Draw a bounding box around every malaria parasite, every leukocyte, and every artifact (stain precipitate or debris).
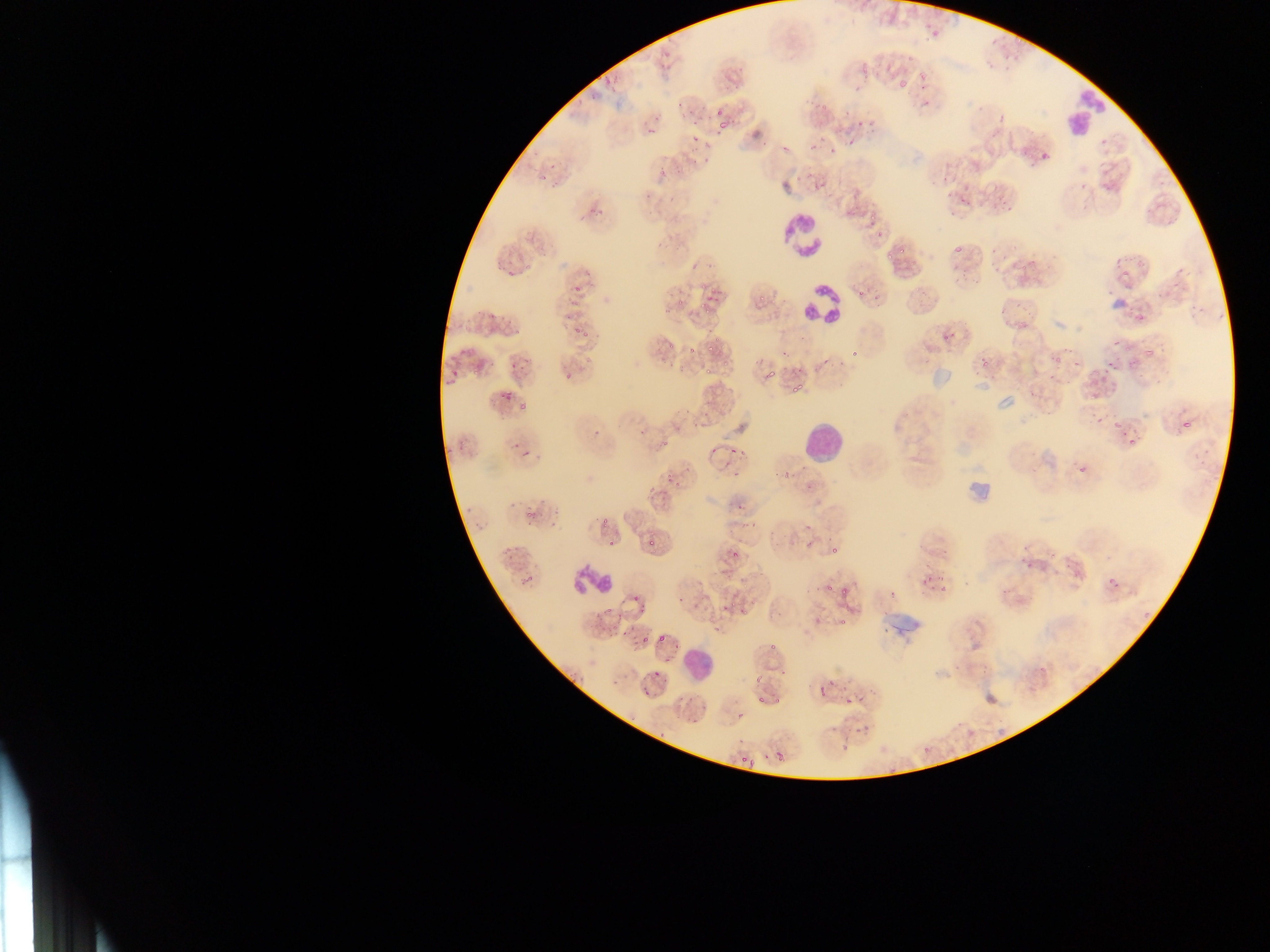

Approximate bounding boxes as left top right bottom in pixels.
Malaria parasites: 921 20 939 44; 886 75 908 94; 708 95 729 115; 812 96 834 115; 686 98 706 118; 645 99 671 132; 698 114 711 132; 714 116 736 134; 851 120 866 130; 804 130 826 156; 826 136 839 159; 844 137 856 151; 690 138 703 150; 1033 145 1055 171; 537 151 565 181; 657 156 675 182; 802 157 811 183; 934 170 954 181; 580 191 613 221; 960 193 973 207; 992 193 1006 208; 869 224 888 246; 953 236 971 260; 1119 267 1136 283; 571 276 585 292; 867 279 880 293; 700 284 714 318; 657 286 670 316; 562 294 591 307; 490 305 500 322; 1131 317 1152 331; 572 320 582 337; 936 325 961 352; 687 337 697 355; 846 340 864 366; 700 345 722 359; 565 351 583 378; 1142 353 1157 363; 1101 357 1123 375; 973 359 1000 378; 507 364 518 377; 445 367 460 380; 760 367 777 379; 1088 374 1114 397; 789 383 811 402; 498 387 514 401; 518 400 528 410; 1176 411 1199 438; 1107 418 1126 429; 1120 423 1144 453; 589 424 604 438; 635 424 645 436; 661 435 679 448; 518 443 532 456; 730 443 752 463; 707 448 719 456; 663 464 681 485; 1076 466 1091 476; 728 471 745 479; 650 480 660 499; 736 500 750 515; 522 514 536 527; 548 514 561 530; 645 533 655 548; 607 534 620 547; 728 547 746 558; 829 547 843 560; 918 569 951 600; 823 580 838 597; 632 586 645 612; 675 587 689 609; 838 589 853 601; 890 591 900 601; 600 600 614 616; 838 603 857 629; 716 604 730 614; 621 618 632 636; 632 629 652 648; 715 629 724 635; 656 630 669 642; 648 667 662 678; 828 672 842 690; 842 678 865 712; 642 684 653 702; 735 710 748 723; 774 748 788 763.
Leukocytes: 1061 81 1102 134; 777 208 830 265; 799 281 843 325; 796 414 850 470; 572 563 617 600; 680 639 720 681.

Summary:
  - Image size: 1270×952 pixels
  - Country: Ghana
  - Capture: mobile-phone photograph through a microscope
  - Field of view: single
  - Preparation: thin blood smear